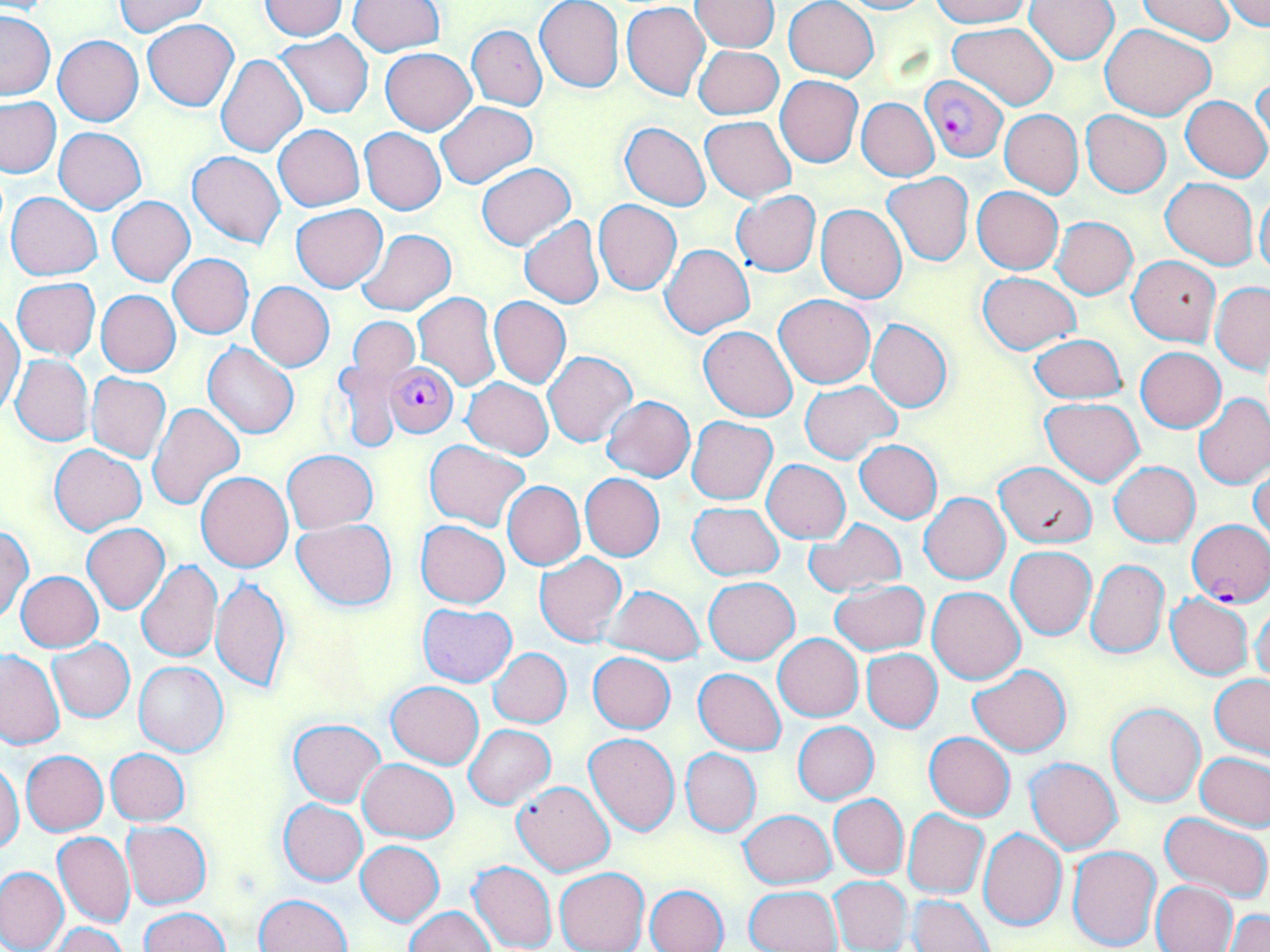

Approximate bounding boxes as [x1, y1, x2, y2] in pixels. Plasmodium falciparum-infected red blood cell locations: [920, 76, 1008, 162], [386, 363, 459, 437], [1187, 520, 1270, 605]. Uninfected red blood cell locations: [115, 0, 210, 37], [535, 0, 623, 92], [784, 0, 878, 81], [830, 0, 933, 14], [930, 0, 1030, 27], [1024, 0, 1119, 63], [1222, 0, 1269, 31], [258, 1, 348, 40], [349, 1, 446, 56], [690, 1, 780, 51], [1135, 1, 1239, 42], [621, 2, 710, 100], [0, 10, 55, 101], [142, 19, 239, 112], [948, 22, 1060, 109], [1102, 23, 1215, 119], [466, 24, 547, 111], [276, 31, 373, 118], [54, 35, 143, 126], [694, 45, 783, 120], [380, 48, 477, 134], [216, 53, 306, 157], [1251, 73, 1269, 162], [776, 76, 863, 168], [1181, 95, 1269, 182], [0, 96, 62, 178], [857, 97, 939, 181], [435, 102, 537, 188], [999, 109, 1083, 197], [1080, 110, 1171, 197], [699, 116, 796, 202], [620, 121, 711, 210], [274, 124, 365, 212], [54, 127, 146, 214], [359, 127, 446, 214], [187, 151, 286, 249], [477, 163, 575, 249], [884, 173, 973, 265], [1161, 178, 1258, 269], [972, 185, 1064, 274], [1256, 187, 1270, 283], [731, 190, 822, 278], [5, 191, 102, 280], [107, 197, 196, 286], [594, 200, 683, 295], [815, 203, 907, 303], [290, 204, 388, 292], [519, 216, 605, 309], [1053, 216, 1138, 299], [357, 229, 456, 316], [659, 243, 755, 338], [169, 253, 254, 338], [1128, 256, 1220, 345], [977, 271, 1079, 355], [11, 278, 101, 359], [1211, 281, 1270, 373], [248, 282, 334, 371], [97, 290, 180, 376], [413, 293, 500, 391], [773, 294, 875, 388], [489, 296, 571, 388], [0, 310, 25, 416], [348, 316, 420, 384], [866, 317, 953, 413], [699, 326, 800, 422], [1030, 334, 1126, 404], [203, 342, 299, 439], [1135, 346, 1226, 432], [543, 351, 636, 446], [10, 354, 94, 447], [331, 361, 405, 454], [87, 372, 171, 463], [463, 378, 554, 460], [799, 381, 901, 463], [1194, 394, 1270, 489], [600, 396, 695, 483], [1039, 397, 1145, 486], [148, 402, 245, 511], [687, 416, 777, 504], [855, 439, 943, 523], [425, 440, 531, 532], [50, 443, 145, 534], [283, 450, 377, 533], [762, 460, 850, 543], [993, 461, 1097, 548], [1109, 462, 1199, 546], [1249, 465, 1270, 550], [196, 471, 293, 572], [580, 474, 665, 561], [503, 481, 585, 569], [919, 493, 1009, 584], [688, 502, 783, 580], [294, 518, 396, 611], [804, 518, 906, 597], [416, 521, 510, 608], [81, 523, 170, 614], [0, 527, 33, 623], [1007, 546, 1097, 639], [534, 552, 626, 646], [1085, 558, 1169, 658], [136, 560, 222, 663], [16, 571, 103, 652], [210, 576, 290, 693], [703, 576, 798, 663], [830, 579, 928, 656], [602, 584, 706, 665], [927, 585, 1025, 685], [1165, 593, 1254, 681], [1251, 600, 1270, 686], [418, 603, 517, 687], [773, 633, 863, 722], [49, 638, 135, 721], [489, 648, 572, 727], [861, 648, 941, 733], [0, 650, 63, 750], [588, 653, 675, 733], [135, 661, 227, 756], [968, 663, 1072, 756], [694, 668, 786, 754], [1210, 674, 1270, 760], [387, 681, 483, 769], [1107, 703, 1205, 807], [288, 718, 385, 805], [793, 720, 878, 804], [465, 724, 556, 808], [583, 732, 679, 835], [925, 732, 1015, 821], [681, 747, 761, 835], [103, 748, 190, 826], [22, 750, 109, 835], [1196, 752, 1270, 830], [1026, 757, 1123, 854], [358, 758, 458, 842], [1, 760, 24, 855], [513, 781, 616, 876], [829, 794, 908, 878], [279, 799, 367, 886], [740, 809, 836, 888], [902, 809, 990, 898], [1159, 811, 1270, 902], [121, 821, 212, 908], [979, 828, 1067, 931], [53, 831, 135, 928], [356, 840, 445, 926], [1068, 845, 1162, 951], [468, 860, 557, 952], [0, 866, 70, 952], [554, 868, 649, 952], [829, 875, 911, 951], [1151, 880, 1239, 952], [645, 884, 730, 952], [744, 885, 842, 951], [910, 893, 993, 952], [253, 894, 352, 952], [405, 906, 495, 952], [142, 908, 230, 952], [1224, 910, 1270, 952], [50, 923, 129, 952]. Slide-level diagnosis: Plasmodium falciparum. 1000x magnification. Light microscopy. May-Grünwald-Giemsa-stained preparation. Thin blood film. One field of a larger specimen. Image is 1270×952 pixels.